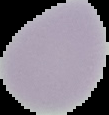
image_type: segmented cell region with the area outside set to black
preparation: thin blood smear
malaria_status: uninfected
image_size: 109×115 pixels